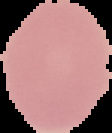
Segmented cell region on a black background. Result: no malaria parasites seen. Image is 112×133 pixels. From a thin blood smear.